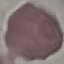

result = no malaria parasites seen
image type = cell patch, automatically extracted from a larger field of view and resized to 64 × 64 pixels
stain = Giemsa
preparation = thin smear
capture = smartphone through the microscope eyepiece